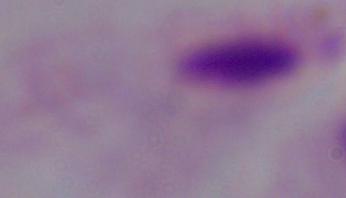
{
  "identification": "trichomonad",
  "modality": "photomicrograph",
  "magnification": "1000x"
}